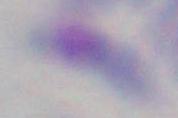

1000x magnification. Photomicrograph. Toxoplasma gondii is seen.